Give the preparation type.
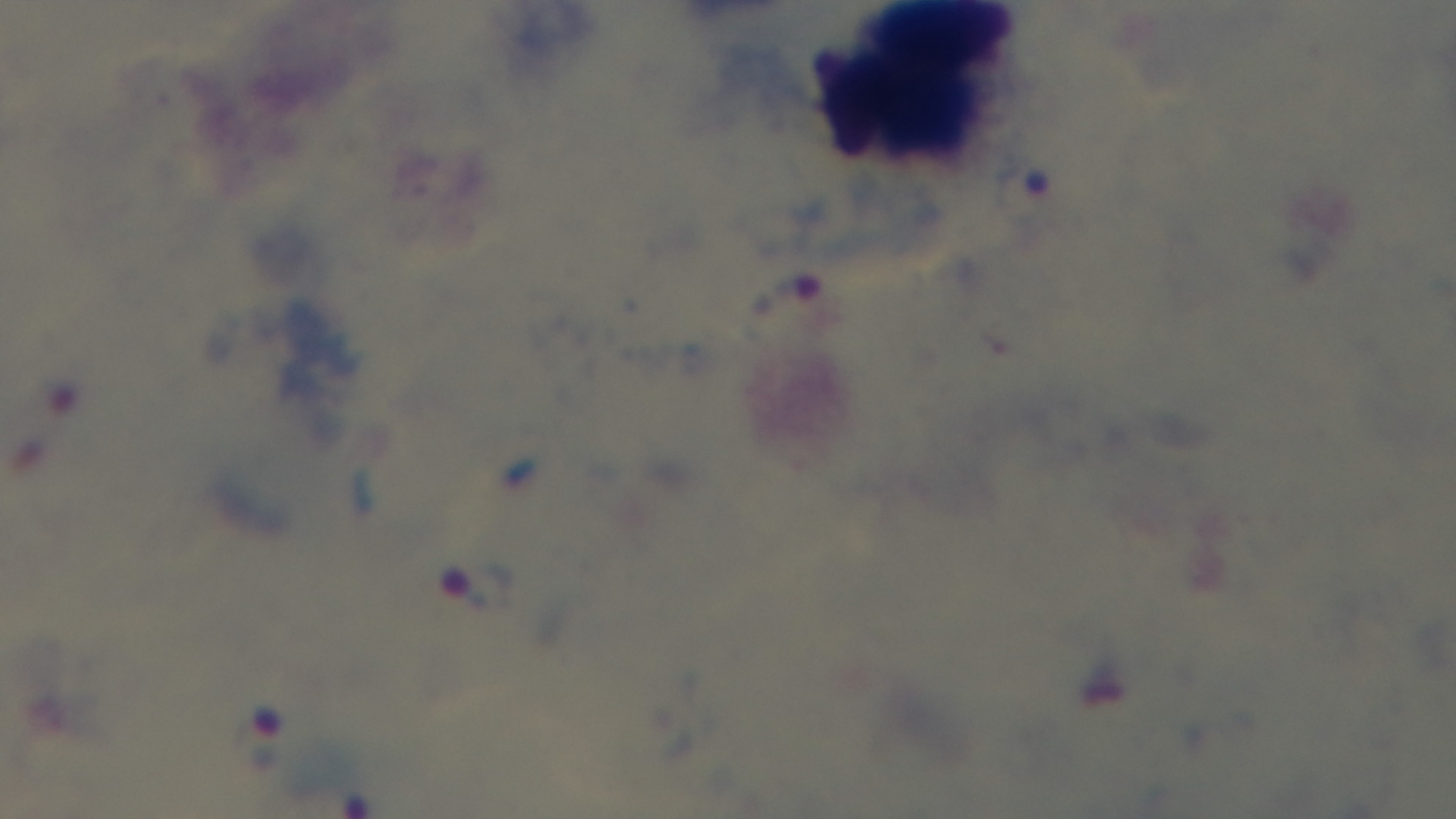
A thick smear.

Mounted 4K digital camera. Giemsa-stained. Malaria status: positive. Oil-immersion objective, 100x. Photomicrograph. Single field of view.